Report the malaria status of this cell.
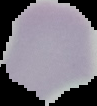

It is uninfected.

Summary:
  - Preparation: thin blood film
  - Image type: segmented cell region with the area outside set to black
  - Image size: 97×106 pixels